Assess this cell for malaria.
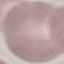

It is uninfected.

Cell patch, automatically extracted from a larger field of view and resized to 64 × 64 pixels. Thin blood film. Photographed with a smartphone camera at the microscope eyepiece. Giemsa-stained preparation.